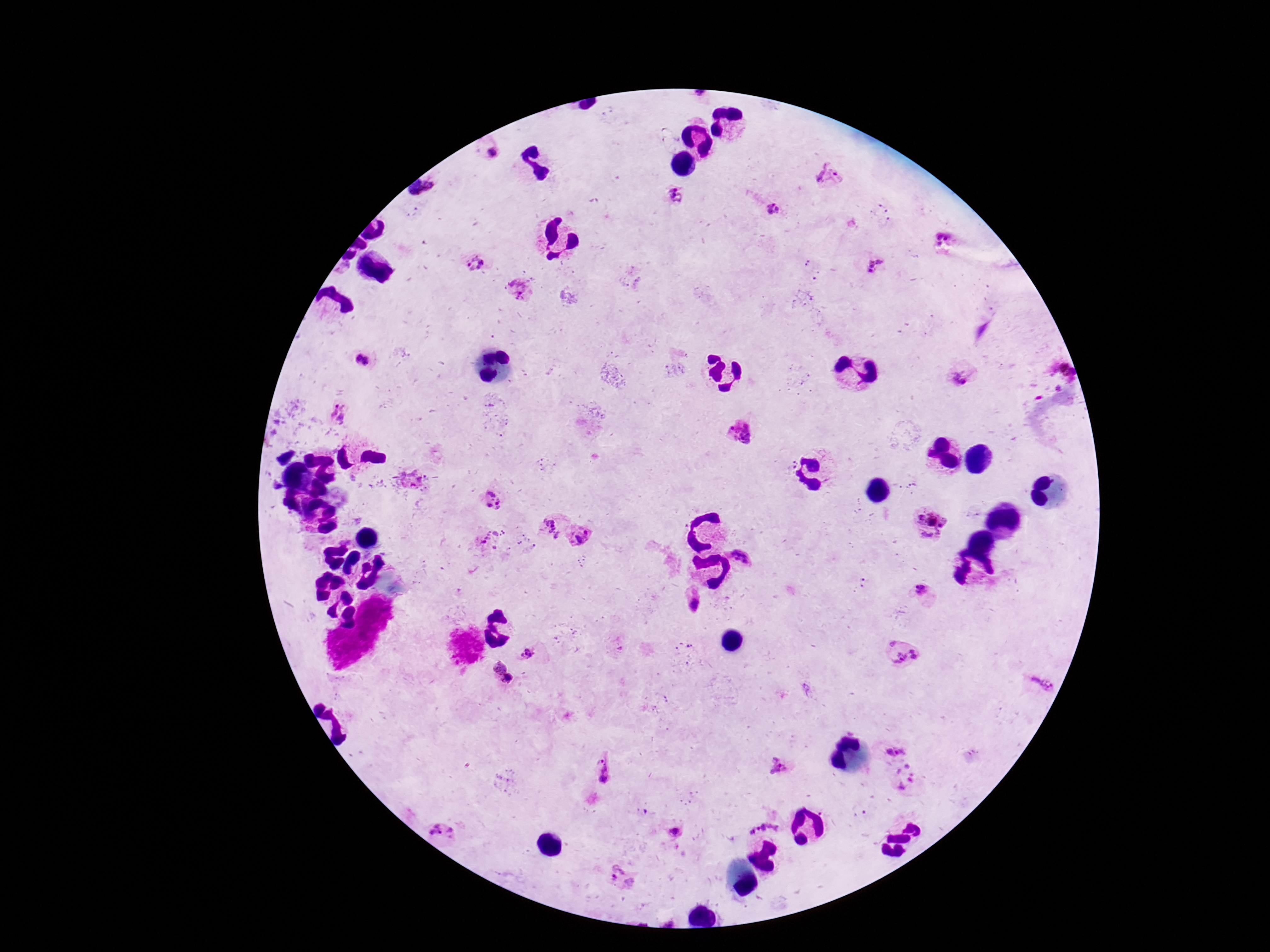
patient malaria status = positive
preparation = thick peripheral-blood smear
capture = smartphone camera through the microscope eyepiece
field of view = single
image size = 1270×952 pixels
magnification = 100x
stain = Giemsa
Plasmodium parasite locations = approximate centers as [x, y] in pixels: [493, 151], [830, 176], [432, 187], [672, 195], [772, 207], [942, 234], [475, 263], [873, 264], [519, 289], [364, 361], [1064, 370], [964, 377], [337, 412], [744, 432], [493, 500], [932, 522], [551, 526], [584, 538], [492, 539], [749, 545], [922, 592], [693, 598], [526, 652], [902, 655], [502, 673], [1040, 681], [893, 746], [779, 764], [602, 769], [905, 779], [765, 819], [446, 828], [676, 832], [621, 876]